Describe the morphology of the red blood cells.
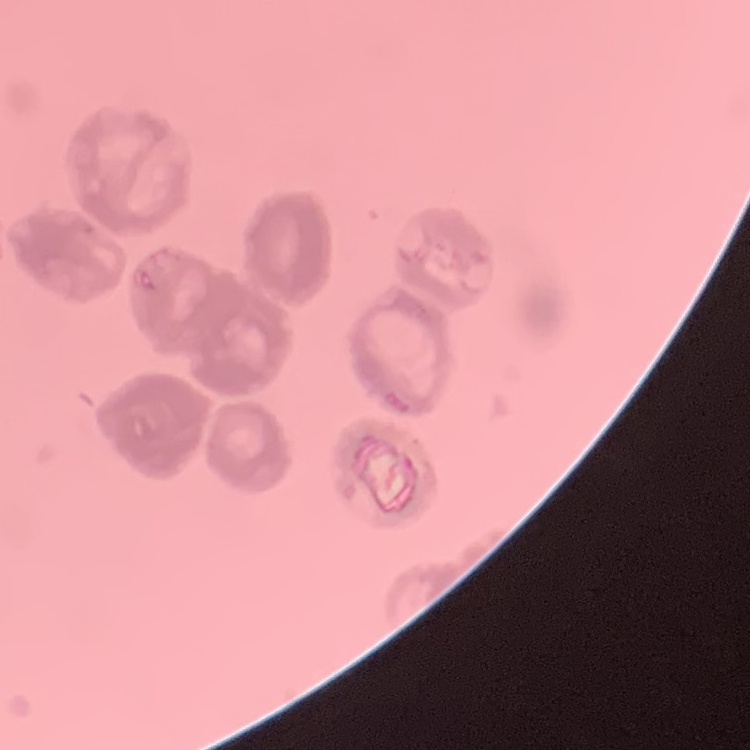

Rouleaux formation.

preparation = thin peripheral smear
stain = Field's or Giemsa
image type = one tile cut from a larger photomicrograph